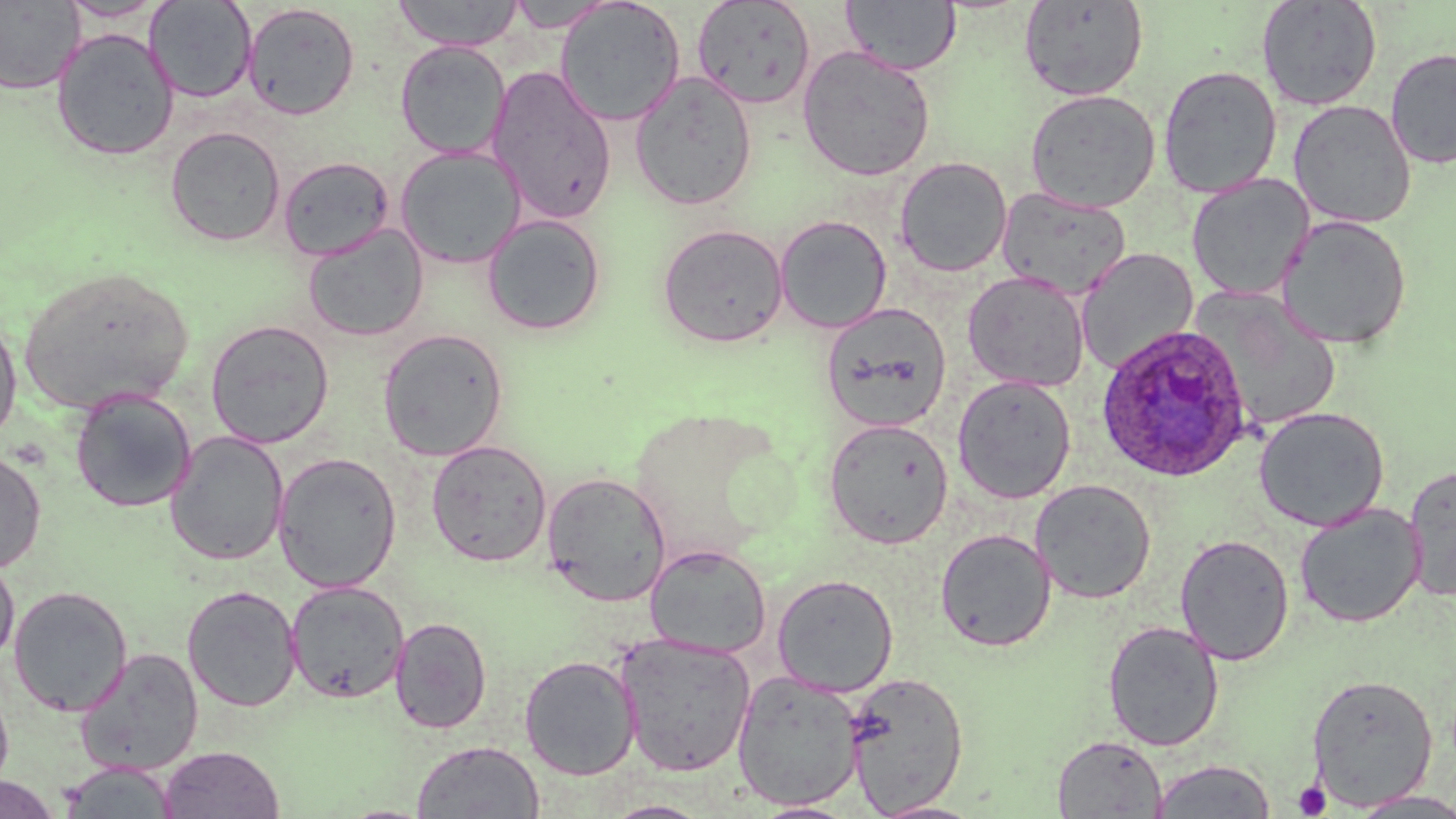

Summary:
  - Coordinate format: approximate bounding boxes as named x1/y1/x2/y2 corners in pixels
  - Uninfected red blood cell locations: (x1=59, y1=0, x2=167, y2=22), (x1=392, y1=0, x2=525, y2=51), (x1=556, y1=0, x2=686, y2=126), (x1=842, y1=0, x2=961, y2=75), (x1=1018, y1=0, x2=1149, y2=101), (x1=1256, y1=0, x2=1383, y2=110), (x1=0, y1=1, x2=84, y2=94), (x1=144, y1=1, x2=256, y2=103), (x1=506, y1=1, x2=616, y2=32), (x1=691, y1=1, x2=817, y2=110), (x1=243, y1=3, x2=360, y2=120), (x1=51, y1=28, x2=179, y2=161), (x1=395, y1=40, x2=509, y2=159), (x1=797, y1=44, x2=936, y2=181), (x1=1385, y1=47, x2=1456, y2=169), (x1=1158, y1=65, x2=1282, y2=198), (x1=487, y1=66, x2=617, y2=225), (x1=629, y1=71, x2=758, y2=210), (x1=1024, y1=88, x2=1161, y2=212), (x1=1288, y1=99, x2=1417, y2=229), (x1=165, y1=125, x2=286, y2=247), (x1=394, y1=146, x2=525, y2=269), (x1=278, y1=156, x2=395, y2=262), (x1=895, y1=156, x2=1012, y2=276), (x1=1186, y1=174, x2=1314, y2=301), (x1=995, y1=186, x2=1132, y2=299), (x1=482, y1=214, x2=607, y2=336), (x1=1276, y1=214, x2=1413, y2=350), (x1=775, y1=215, x2=892, y2=333), (x1=656, y1=223, x2=790, y2=348), (x1=303, y1=224, x2=428, y2=342), (x1=1076, y1=248, x2=1198, y2=374), (x1=15, y1=264, x2=196, y2=416), (x1=962, y1=271, x2=1090, y2=392), (x1=1191, y1=287, x2=1342, y2=435), (x1=821, y1=302, x2=952, y2=432), (x1=0, y1=314, x2=22, y2=446), (x1=205, y1=319, x2=334, y2=449), (x1=377, y1=328, x2=509, y2=461), (x1=952, y1=375, x2=1076, y2=504), (x1=70, y1=389, x2=196, y2=512), (x1=1253, y1=406, x2=1390, y2=531), (x1=823, y1=418, x2=954, y2=549), (x1=166, y1=430, x2=289, y2=566), (x1=426, y1=439, x2=552, y2=567), (x1=0, y1=450, x2=46, y2=574), (x1=273, y1=452, x2=402, y2=593), (x1=1403, y1=462, x2=1456, y2=601), (x1=541, y1=472, x2=672, y2=606), (x1=1029, y1=478, x2=1157, y2=604), (x1=1294, y1=503, x2=1425, y2=628), (x1=935, y1=528, x2=1056, y2=652), (x1=1174, y1=533, x2=1294, y2=665), (x1=645, y1=543, x2=771, y2=658), (x1=0, y1=552, x2=20, y2=667), (x1=772, y1=572, x2=899, y2=696), (x1=285, y1=580, x2=409, y2=703), (x1=181, y1=584, x2=303, y2=712), (x1=8, y1=585, x2=132, y2=716), (x1=390, y1=616, x2=492, y2=734), (x1=1102, y1=620, x2=1224, y2=751), (x1=616, y1=634, x2=756, y2=777), (x1=75, y1=647, x2=204, y2=776), (x1=519, y1=654, x2=641, y2=779), (x1=731, y1=670, x2=865, y2=810), (x1=844, y1=670, x2=969, y2=815), (x1=1306, y1=673, x2=1439, y2=810), (x1=0, y1=683, x2=14, y2=792), (x1=1052, y1=735, x2=1167, y2=818), (x1=411, y1=741, x2=545, y2=818), (x1=159, y1=745, x2=285, y2=818), (x1=1150, y1=759, x2=1275, y2=818), (x1=58, y1=760, x2=180, y2=818), (x1=0, y1=775, x2=62, y2=819), (x1=1348, y1=790, x2=1456, y2=818), (x1=600, y1=799, x2=715, y2=819), (x1=869, y1=799, x2=986, y2=818), (x1=751, y1=800, x2=860, y2=818)
  - Platelet locations: (x1=1293, y1=780, x2=1331, y2=817)
  - Plasmodium ovale-infected red blood cell locations: (x1=1095, y1=324, x2=1253, y2=483)
  - Slide-level diagnosis: Plasmodium ovale
  - Modality: optical microscopy
  - Preparation: thin blood smear
  - Field of view: one of a larger specimen
  - Image size: 1456×819 pixels
  - Magnification: 1000x
  - Stain: May-Grünwald-Giemsa